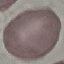 Malaria status: uninfected. Thin smear of blood. Acquired by smartphone through the microscope eyepiece. Giemsa-stained preparation. Automatically extracted cell patch, resized to 64 × 64 pixels.